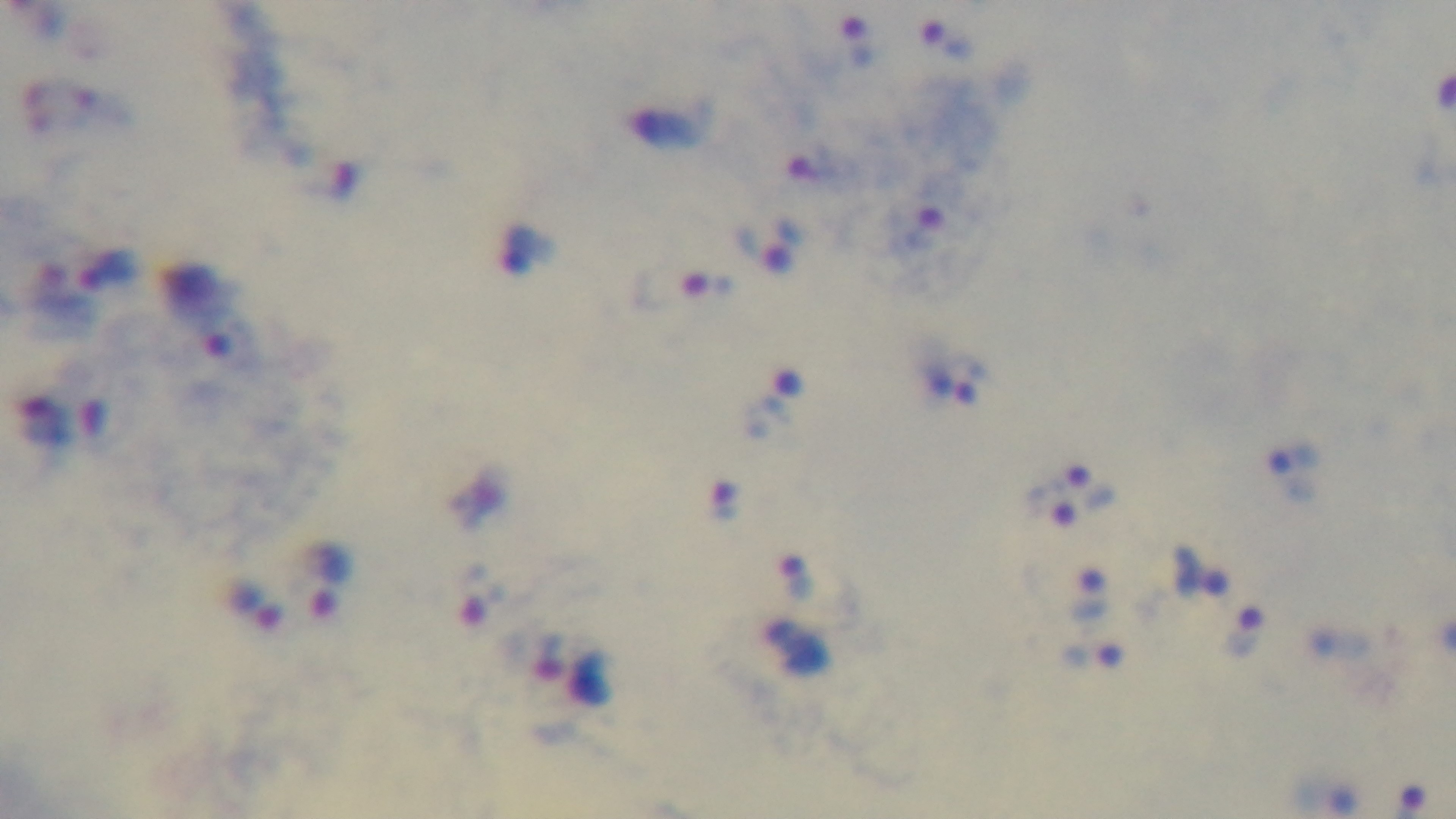
Summary:
  - Field of view: single
  - Objective: 100x oil immersion
  - Preparation: thick blood film
  - Capture: mounted 4K digital camera
  - Modality: light microscopy
  - Malaria status: positive
  - Stain: Giemsa